Identify the parasite.
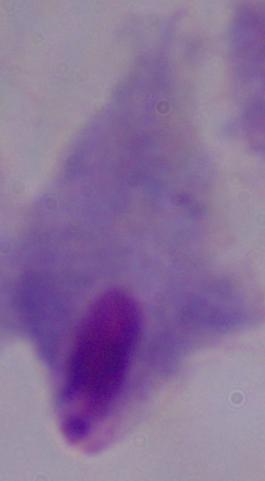
A trichomonad.

Summary:
  - Magnification: 1000x
  - Modality: photomicrograph